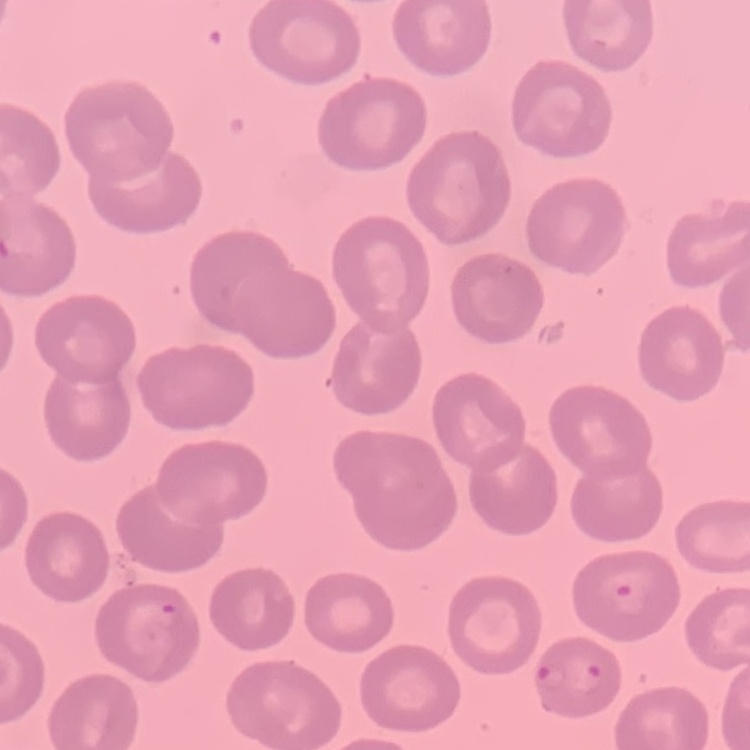

{
  "red_blood_cell_morphology": "no rouleaux formation",
  "preparation": "thin blood smear",
  "image_type": "square crop of a larger photomicrograph",
  "stain": "Field's or Giemsa"
}